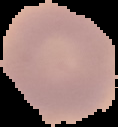
{
  "image_size": "118×127 pixels",
  "result": "no malaria parasites seen",
  "image_type": "cell region segmented out of the field of view; surrounding area masked to black",
  "preparation": "thin blood film"
}